Report the malaria status of this cell.
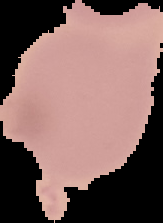
Uninfected.

Segmented cell region on a black background. Image is 163×223 pixels. From a thin blood smear.